Name the parasite shown.
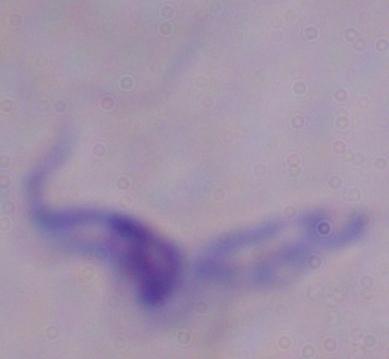
This is a trypanosome.

magnification: 1000x
modality: micrograph